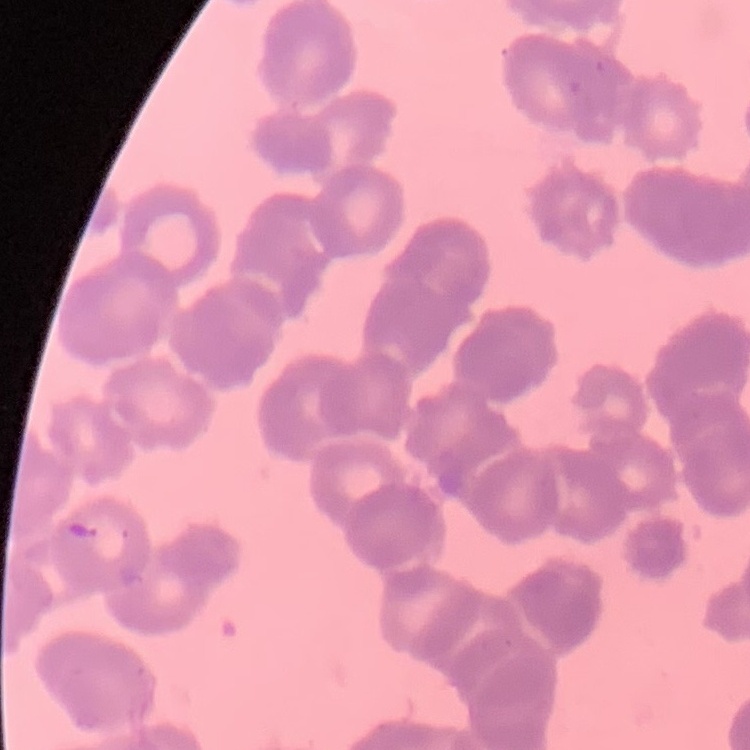

{
  "erythrocyte_morphology": "rouleaux formation",
  "preparation": "thin blood film",
  "image_type": "square crop of a larger photomicrograph",
  "stain": "Field's or Giemsa"
}